Name the parasite shown.
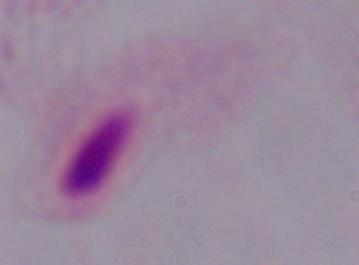
A trichomonad.

{
  "magnification": "1000x",
  "modality": "micrograph"
}